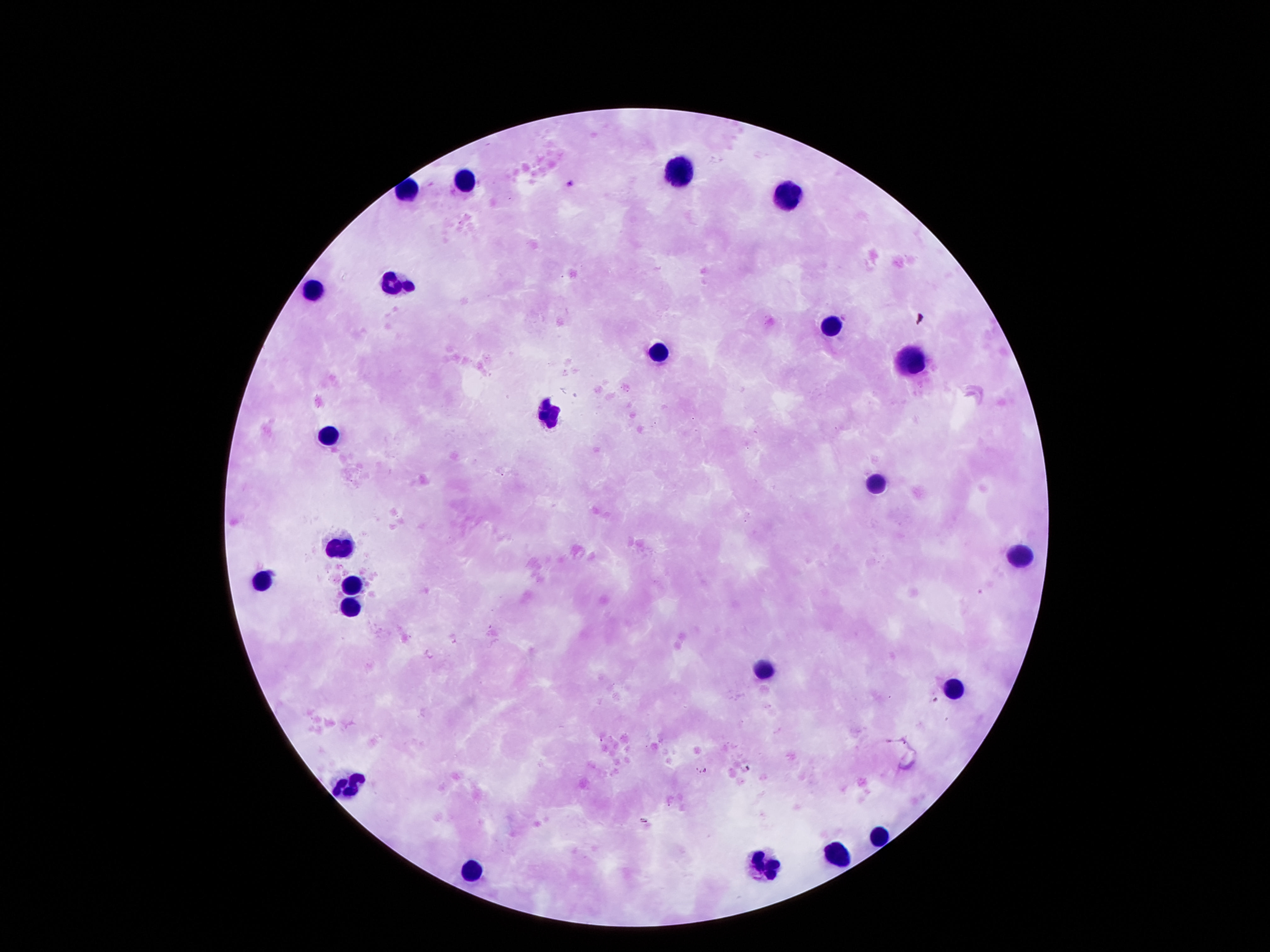
Approximate object centers, in pixels from the top-left corner. Leukocyte locations: (x=678, y=167), (x=463, y=179), (x=775, y=193), (x=395, y=281), (x=311, y=290), (x=829, y=328), (x=654, y=355), (x=909, y=362), (x=547, y=409), (x=325, y=431), (x=873, y=479), (x=338, y=540), (x=1017, y=550), (x=258, y=580), (x=355, y=582), (x=348, y=606), (x=762, y=664), (x=950, y=684), (x=345, y=784), (x=879, y=832), (x=836, y=855), (x=758, y=864), (x=469, y=869). 100x magnification. Photographed through the microscope eyepiece with a smartphone camera. Image is 1270×952 pixels. Giemsa-stained preparation. Thick peripheral-blood smear. Patient malaria status: negative. Single field of view.